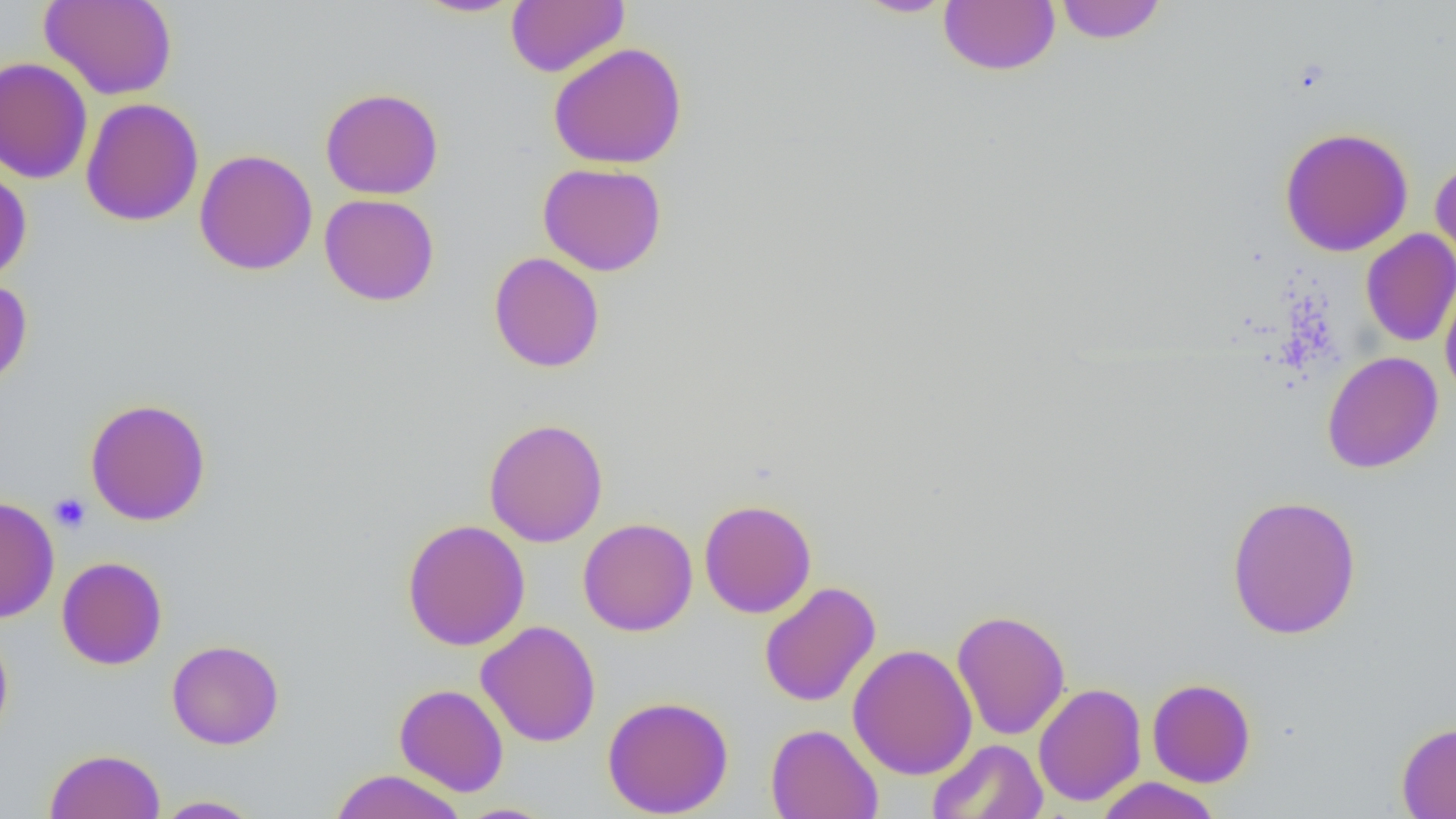
Summary:
  - Coordinate format: approximate bounding boxes as (x1, y1, x2, y2) in pixels
  - Uninfected red blood cell locations: (39, 0, 177, 100), (412, 0, 524, 18), (506, 0, 629, 78), (853, 0, 958, 18), (1053, 0, 1167, 44), (939, 1, 1060, 75), (547, 42, 687, 169), (0, 57, 93, 184), (320, 87, 444, 200), (80, 97, 204, 226), (1278, 125, 1414, 257), (194, 149, 318, 275), (1429, 157, 1456, 276), (538, 162, 667, 276), (0, 166, 32, 285), (319, 193, 439, 306), (1360, 229, 1456, 347), (489, 252, 605, 372), (1440, 272, 1456, 403), (0, 278, 33, 391), (1322, 351, 1443, 473), (84, 398, 212, 526), (483, 416, 608, 548), (1226, 494, 1362, 641), (0, 495, 59, 624), (699, 499, 817, 618), (402, 518, 531, 651), (577, 518, 698, 636), (56, 556, 167, 670), (759, 581, 881, 707), (951, 609, 1070, 741), (476, 620, 601, 747), (0, 624, 14, 747), (167, 639, 284, 750), (847, 643, 977, 781), (1146, 678, 1256, 788), (394, 683, 509, 796), (1033, 683, 1147, 807), (602, 695, 734, 818), (1396, 720, 1456, 818), (766, 723, 883, 819), (927, 738, 1048, 819), (44, 748, 165, 819), (329, 769, 468, 819), (1094, 777, 1223, 819), (152, 795, 263, 818), (453, 803, 561, 819)
  - Platelet locations: (50, 492, 91, 532)
  - Slide-level diagnosis: no evidence of blood parasites
  - Preparation: thin blood film
  - Magnification: 1000x
  - Field of view: one of a larger specimen
  - Image size: 1456×819 pixels
  - Modality: optical microscopy